Point out each leukocyte.
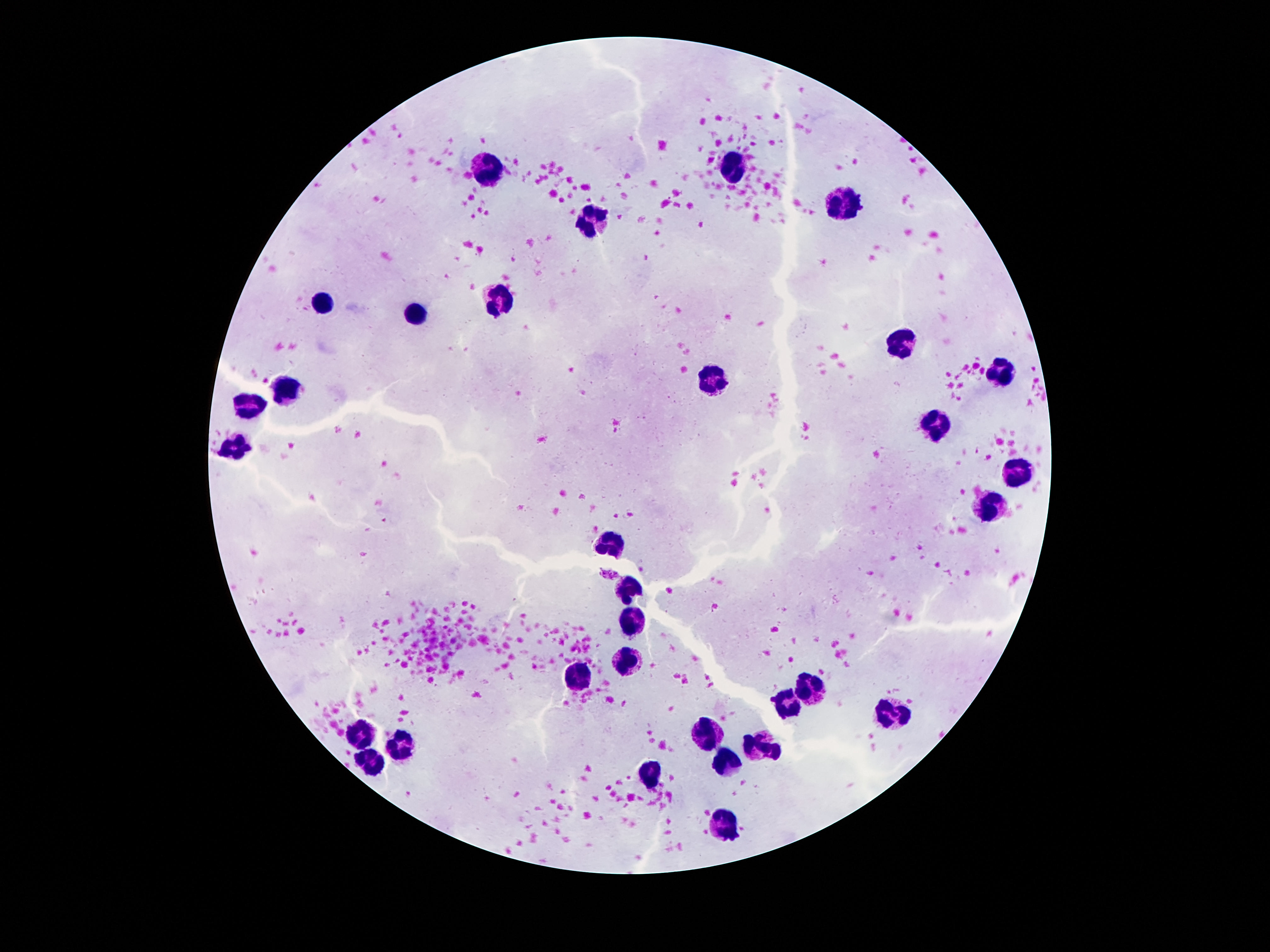
Approximate centers as {x, y} in pixels.
Leukocytes: {727, 169}, {486, 170}, {843, 202}, {594, 221}, {498, 300}, {324, 301}, {420, 314}, {903, 343}, {1001, 374}, {715, 378}, {286, 390}, {248, 408}, {939, 423}, {238, 449}, {1016, 474}, {989, 507}, {612, 544}, {627, 586}, {632, 622}, {627, 660}, {579, 678}, {812, 688}, {788, 704}, {884, 714}, {363, 736}, {708, 738}, {401, 743}, {763, 746}, {375, 763}, {730, 765}, {649, 774}, {727, 827}.

Smartphone photograph taken through the microscope eyepiece. Thick peripheral-blood smear. Giemsa-stained preparation. 100x magnification. Image is 1270×952 pixels. One field from this slide. Patient malaria status: negative.